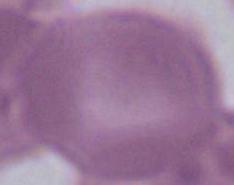
Summary:
  - Identification: red blood cell
  - Magnification: 1000x
  - Modality: photomicrograph